Describe the morphology of the erythrocytes.
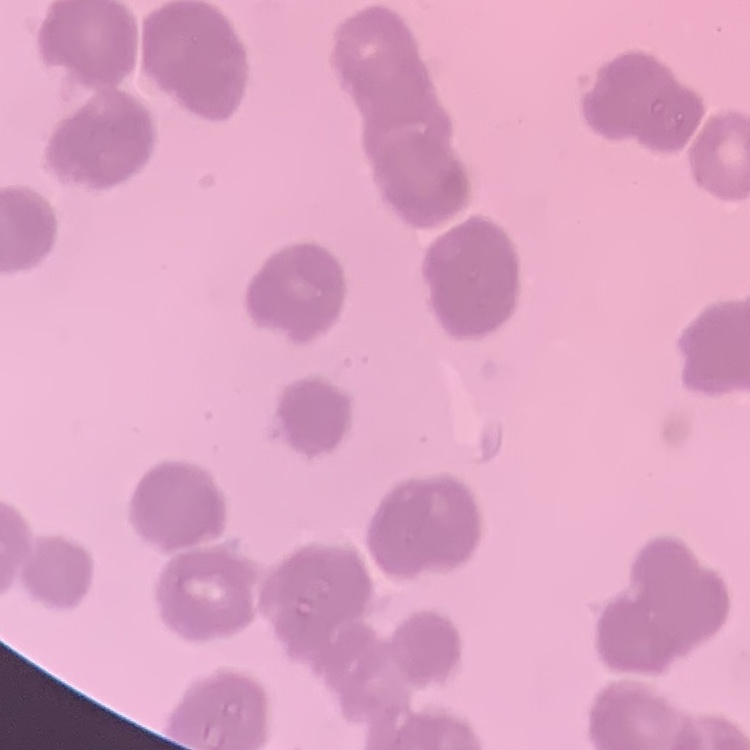
Rouleaux formation.

One tile cut from a larger photomicrograph. Stained with either Field's or Giemsa. Thin peripheral smear.